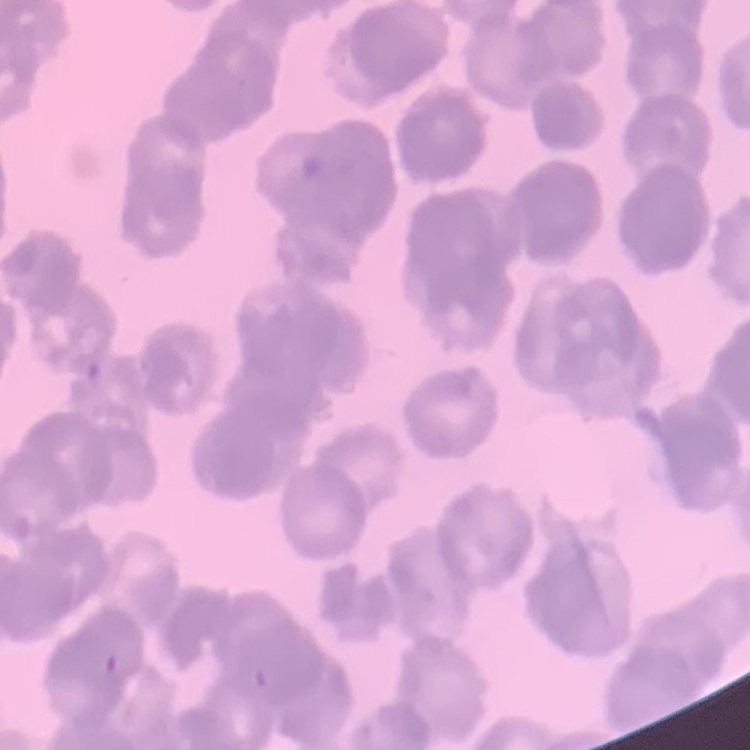
Summary:
  - Red blood cell morphology: rouleaux formation
  - Preparation: thin peripheral smear
  - Stain: Field's or Giemsa
  - Image type: one tile cut from a larger photomicrograph